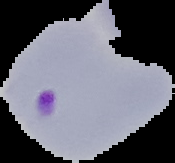 From a thin blood film. Image is 175×163 pixels. The area outside the segmented cell region is set to black. Result: malaria parasites identified.